Identify the preparation type.
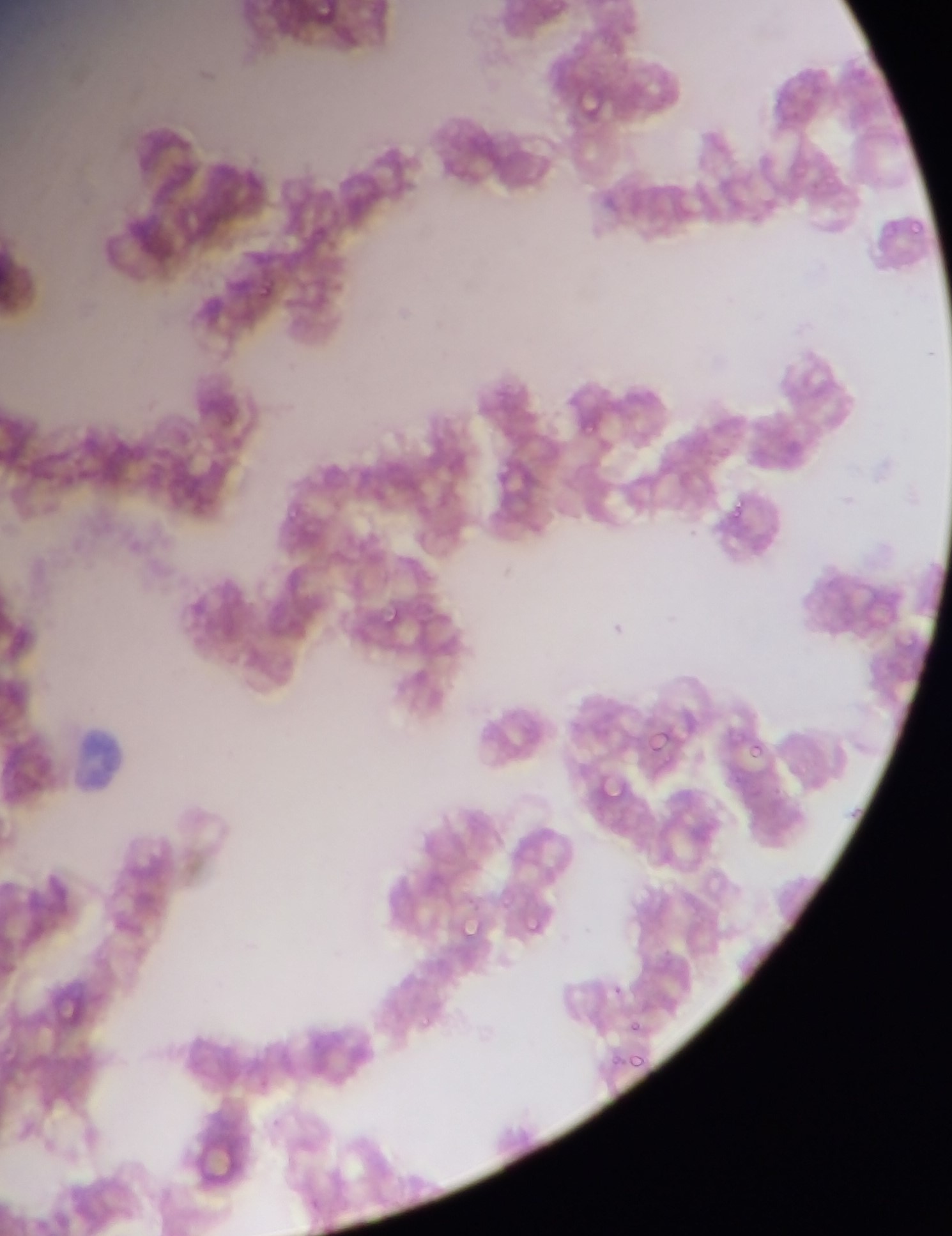

This is a thin smear.

field of view = single
malaria parasite locations = approximate bounding boxes as left top right bottom in pixels: 251 278 283 309; 571 410 597 428; 727 489 767 531; 378 602 405 627; 645 725 680 755; 743 738 768 761; 590 773 629 805; 528 904 559 927; 455 918 483 943; 43 990 104 1022; 626 1019 644 1028; 624 1054 648 1070
image size = 952×1236 pixels
capture = mobile-phone photograph through a microscope
country = Ghana